Classify this cell by malaria status.
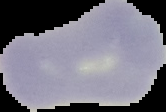

It is uninfected.

The area outside the segmented cell region is set to black. From a thin blood smear. Image is 166×112 pixels.